Identify the cell.
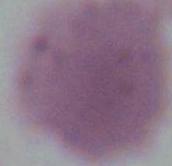

An erythrocyte.

Photomicrograph. Captured at 1000x magnification.